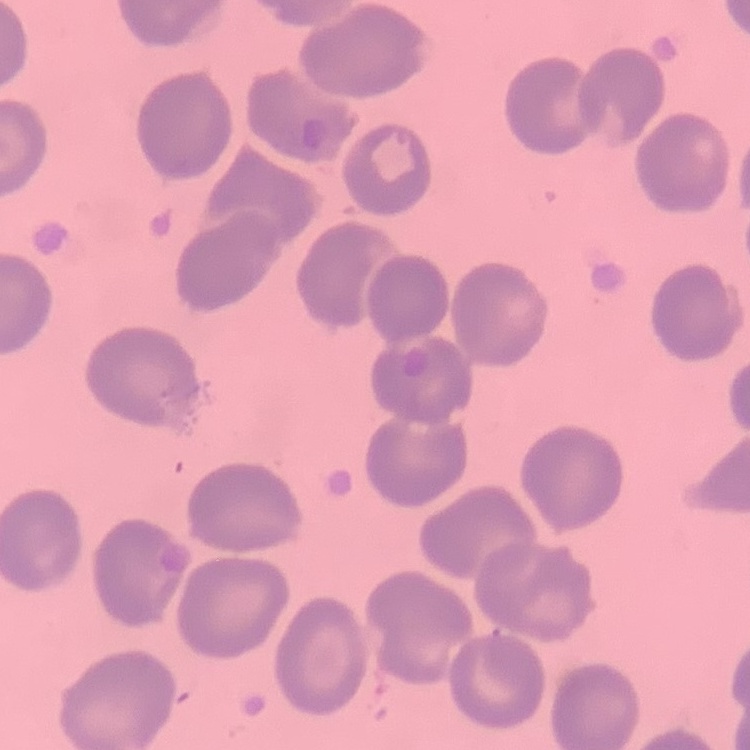
Summary:
  - Erythrocyte morphology: no rouleaux formation
  - Image type: square crop of a larger photomicrograph
  - Preparation: thin blood smear
  - Stain: Field's or Giemsa